Classify this cell by malaria status.
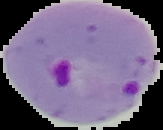
Parasitized.

From a thin blood film. Image is 163×130 pixels. Cell region segmented out of the field of view; the surrounding area is masked to black.